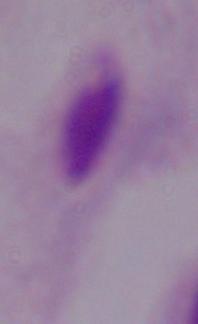

Summary:
  - Identification: trichomonad
  - Magnification: 1000x
  - Modality: photomicrograph